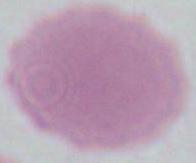

Summary:
  - Magnification: 1000x
  - Modality: photomicrograph
  - Identification: red blood cell